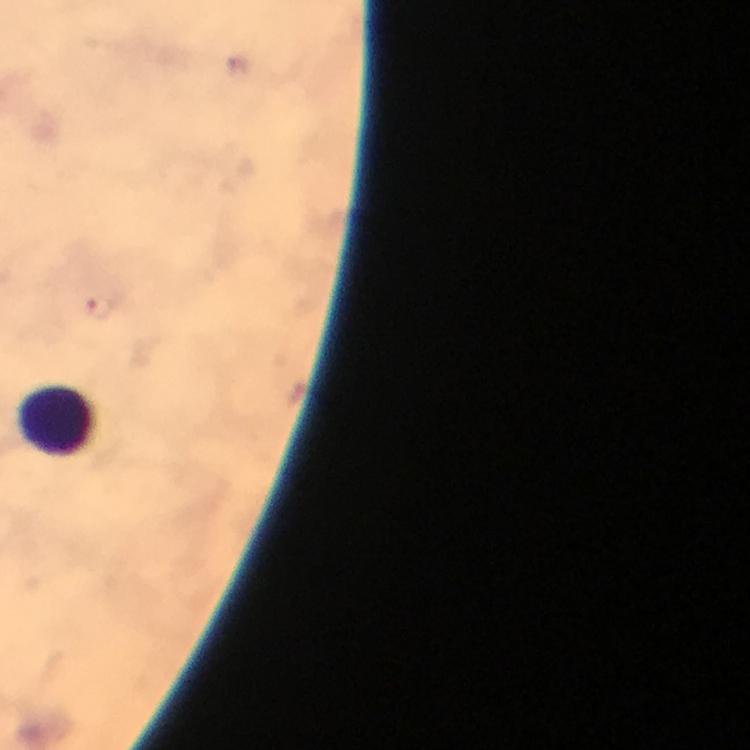

magnification = 100x
context = from a malaria diagnostic workup
capture = smartphone camera through the microscope
preparation = thick blood film
Plasmodium parasite locations = approximate centers as [x, y] in pixels: [99, 308]
image size = 750×750 pixels
cropped from = a single field of view
stain = Giemsa
immersion oil = applied
leukocyte locations = approximate centers as [x, y] in pixels: [58, 422]